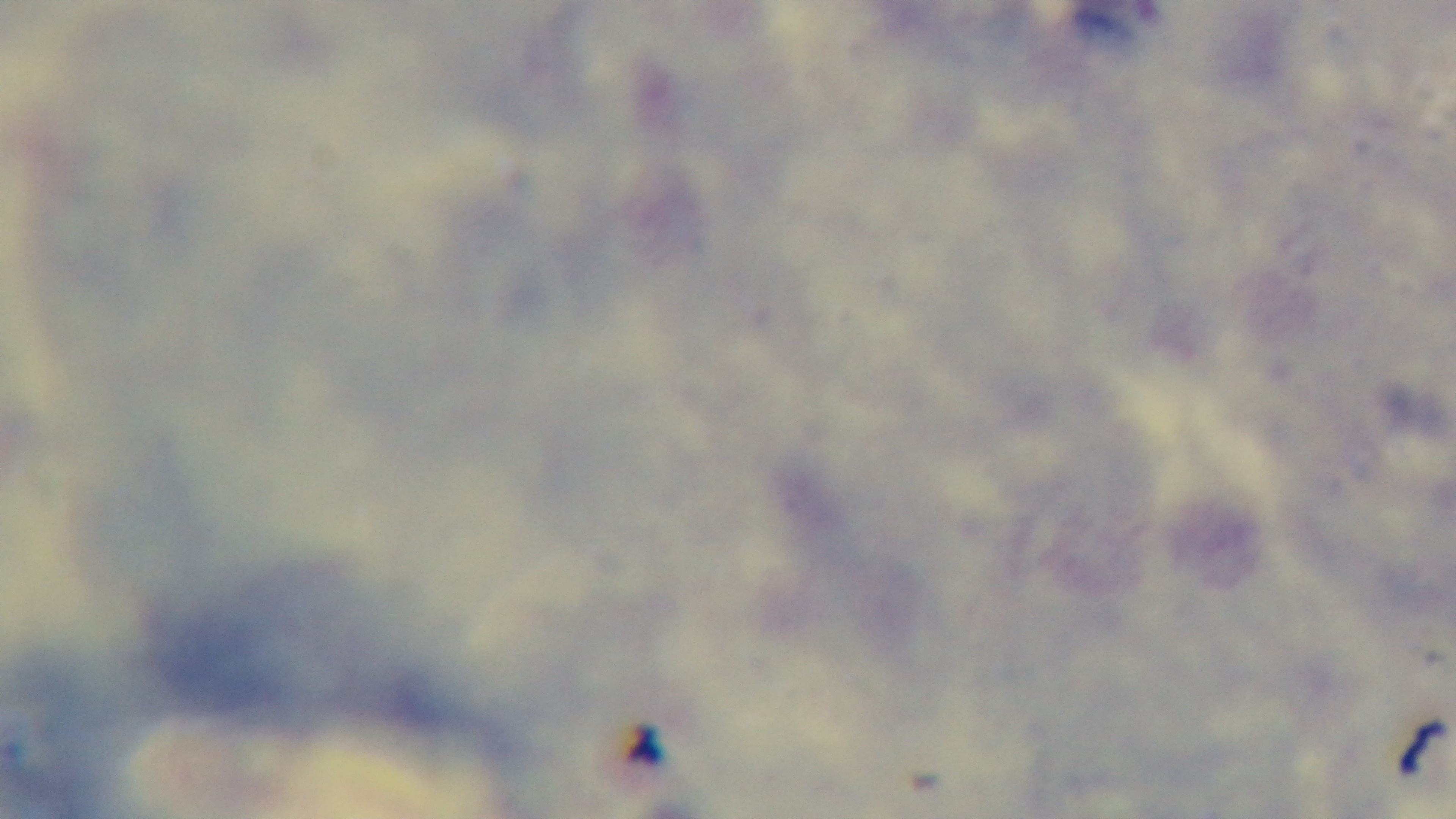

Summary:
  - Stain: Giemsa
  - Capture: mounted 4K digital camera
  - Objective: 100x oil immersion
  - Modality: light microscopy
  - Field of view: single
  - Preparation: thick
  - Malaria status: negative